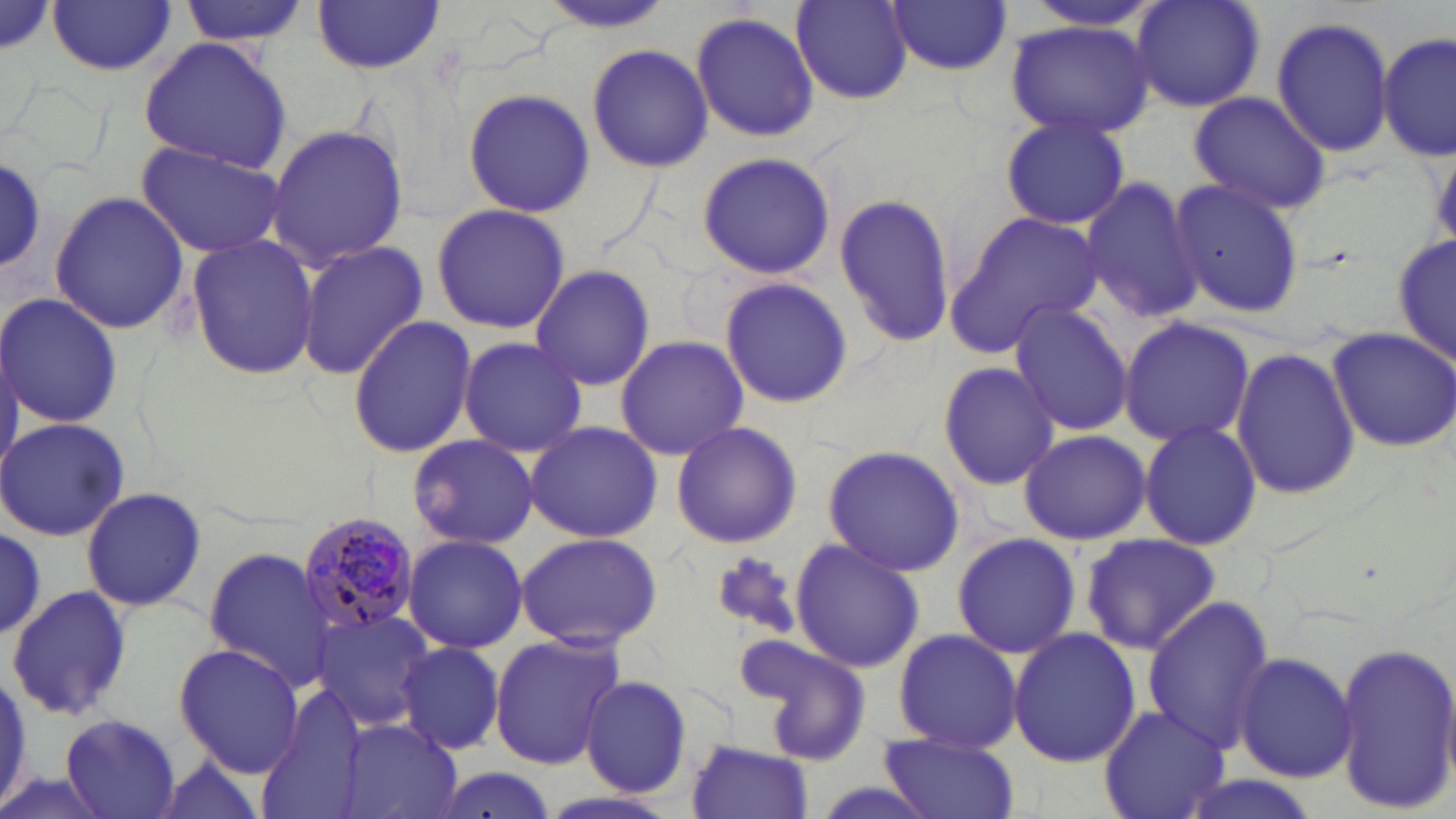
Plasmodium malariae-infected red blood cell locations = approximate bounding boxes as (x1, y1, x2, y2) in pixels: (302, 515, 421, 634)
slide-level diagnosis = Plasmodium malariae
stain = May-Grünwald-Giemsa
image size = 1456×819 pixels
modality = optical microscopy
magnification = 1000x
uninfected red blood cell locations = approximate bounding boxes as (x1, y1, x2, y2) in pixels: (178, 0, 309, 50), (1129, 0, 1267, 112), (791, 1, 914, 103), (1013, 1, 1165, 32), (48, 2, 177, 76), (309, 2, 447, 75), (535, 2, 675, 34), (886, 2, 1012, 75), (689, 11, 819, 142), (1271, 15, 1394, 159), (1006, 21, 1152, 135), (1378, 32, 1453, 162), (138, 37, 293, 175), (586, 42, 712, 173), (464, 86, 592, 216), (1187, 92, 1331, 213), (998, 110, 1131, 230), (263, 123, 408, 269), (134, 139, 289, 261), (63, 150, 240, 308), (695, 151, 837, 281), (0, 156, 46, 271), (1080, 175, 1208, 325), (1168, 178, 1306, 318), (832, 189, 957, 347), (48, 191, 190, 336), (430, 203, 571, 334), (944, 211, 1103, 361), (188, 233, 320, 380), (1393, 234, 1455, 371), (297, 241, 428, 379), (529, 264, 657, 392), (719, 276, 852, 410), (1, 291, 122, 429), (1007, 301, 1135, 437), (347, 313, 477, 458), (1118, 316, 1254, 448), (1327, 324, 1456, 452), (614, 335, 748, 461), (457, 336, 588, 457), (1231, 346, 1359, 500), (937, 360, 1061, 492), (0, 418, 129, 540), (669, 420, 803, 549), (1139, 421, 1262, 549), (524, 422, 663, 541), (1017, 428, 1150, 544), (407, 434, 541, 551), (824, 445, 964, 574), (78, 487, 207, 612), (0, 523, 48, 637), (515, 532, 664, 648), (949, 533, 1083, 660), (1079, 533, 1221, 654), (403, 534, 527, 653), (789, 538, 922, 674), (202, 547, 340, 690), (6, 584, 131, 723), (1139, 596, 1277, 754), (310, 609, 439, 731), (890, 627, 1024, 754), (1007, 628, 1141, 767), (488, 631, 623, 770), (742, 635, 873, 762), (1331, 640, 1456, 815), (397, 641, 506, 755), (173, 642, 303, 776), (1233, 650, 1358, 783), (0, 670, 30, 816), (580, 676, 692, 796), (252, 686, 367, 817), (1099, 704, 1229, 819), (60, 711, 183, 817), (341, 719, 462, 819), (879, 733, 1020, 819), (687, 738, 813, 819), (147, 754, 273, 819)
field of view = single
preparation = thin blood film